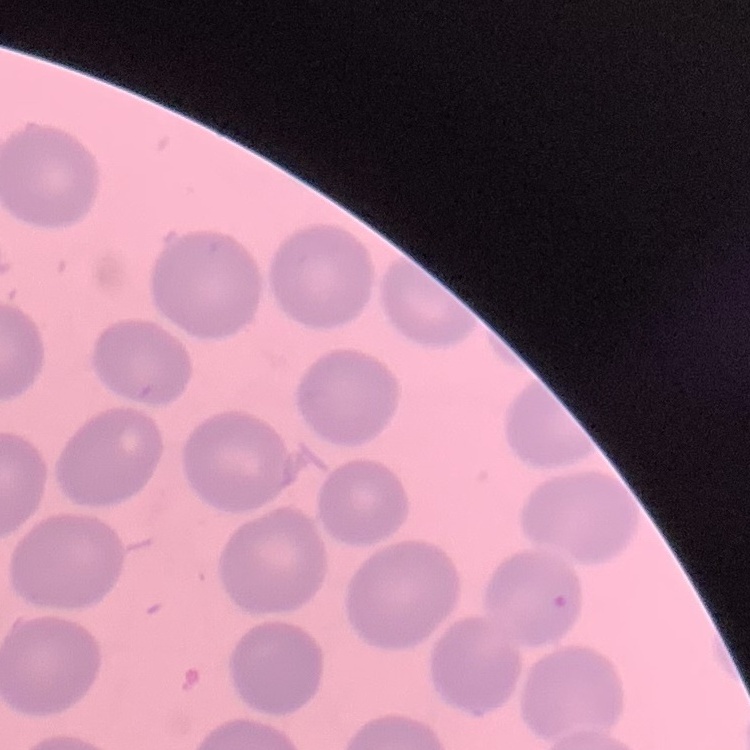

Summary:
  - Erythrocyte morphology: no rouleaux formation
  - Stain: Field's or Giemsa
  - Preparation: thin blood smear
  - Image type: square crop of a larger photomicrograph